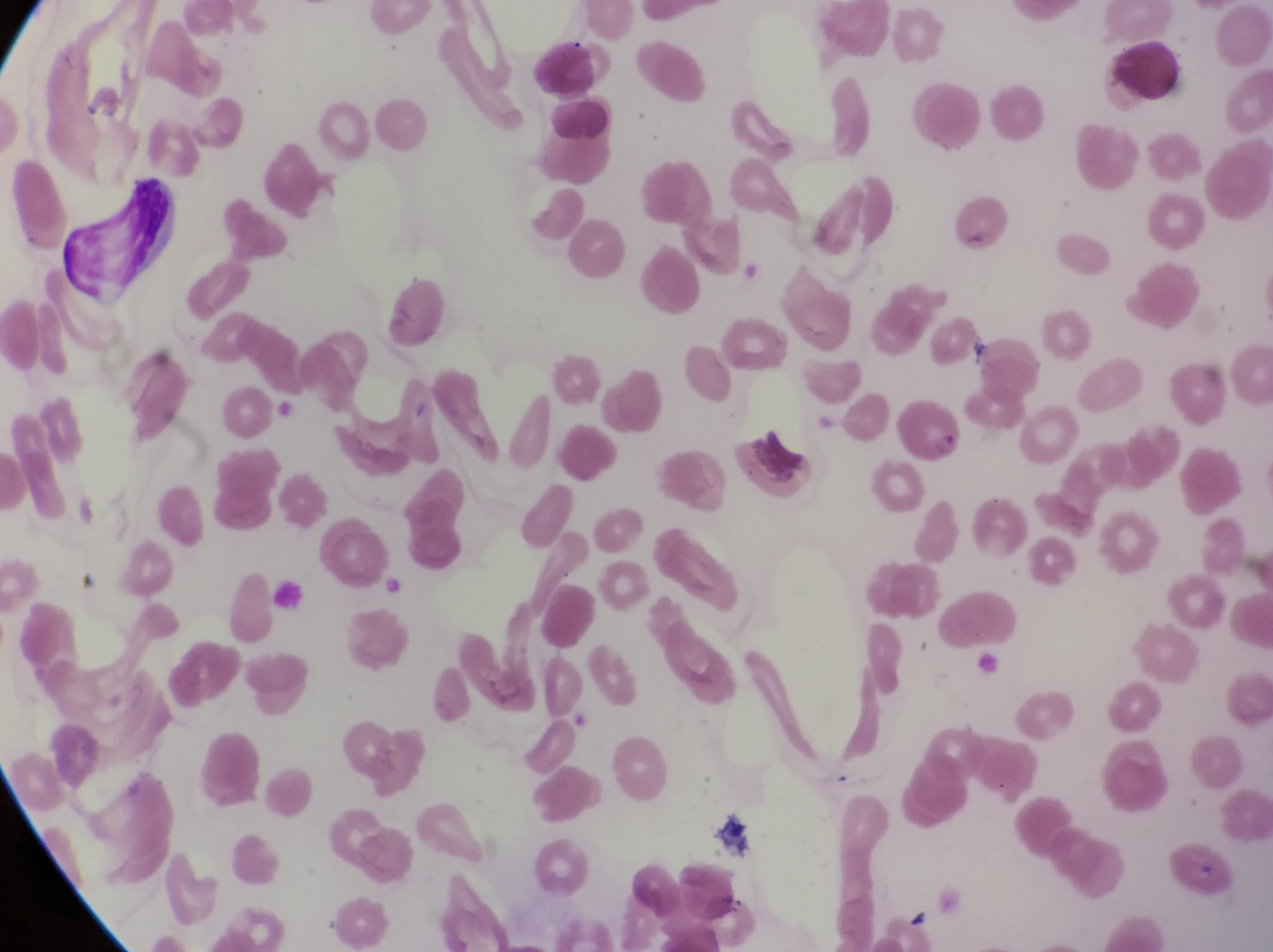

Approximate bounding boxes as left top right bottom in pixels.
Summary:
  - Parasitised red blood cell locations: 899 392 966 464
  - Leukocyte locations: 522 35 607 100; 1106 37 1184 104; 541 97 615 147
  - Field of view: single
  - Country: Uganda
  - Magnification: 1000x
  - Image size: 1273×952 pixels
  - Capture: smartphone photograph through the eyepiece of an Olympus CX-23 microscope
  - Preparation: thin blood smear